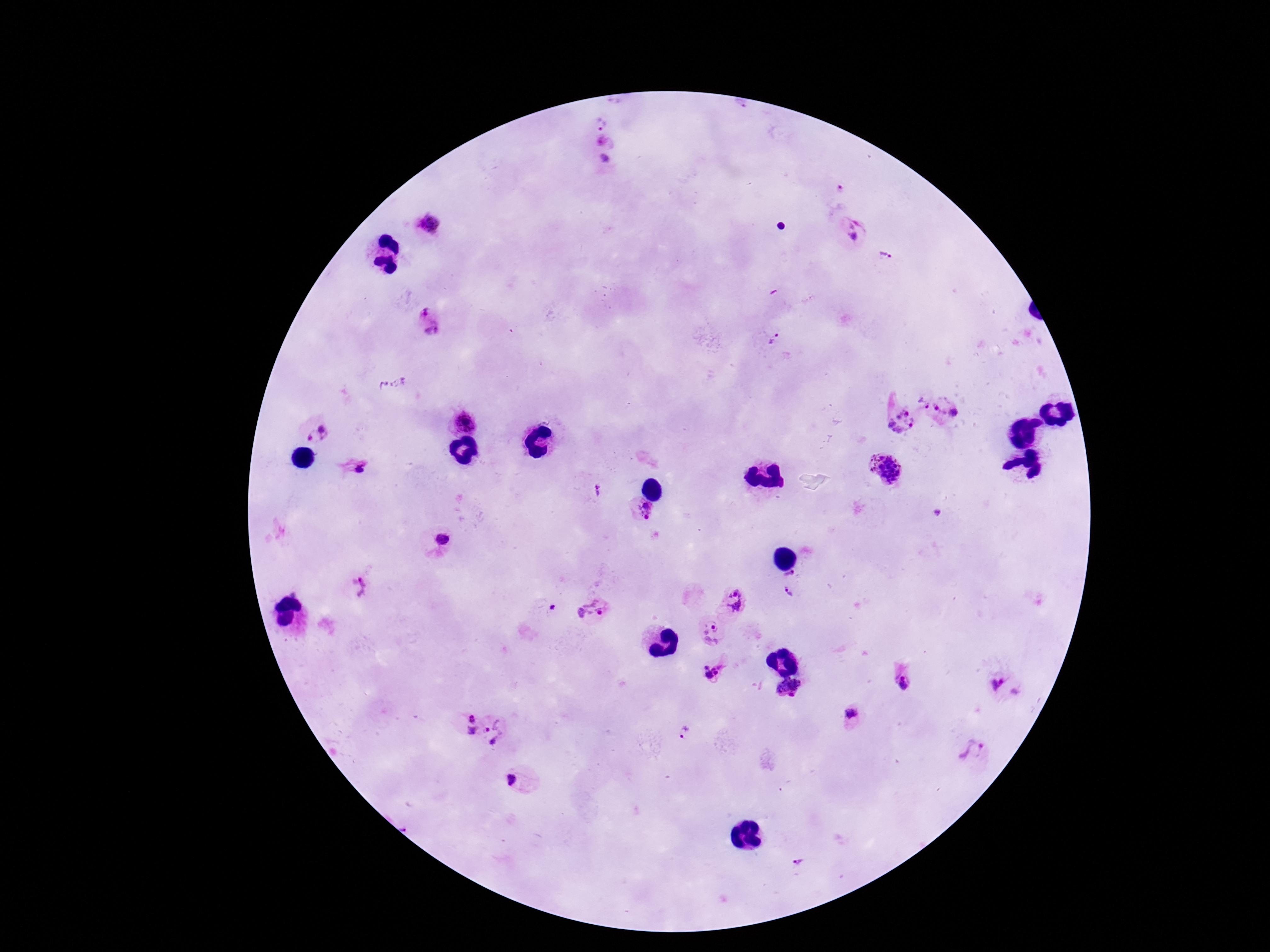

Approximate centers as [x, y] in pixels.
Summary:
  - Plasmodium parasite locations: [601, 124], [605, 160], [428, 224], [852, 229], [885, 256], [423, 312], [432, 329], [774, 337], [923, 402], [937, 407], [954, 413], [463, 421], [900, 421], [322, 428], [315, 439], [356, 467], [884, 469], [598, 491], [638, 512], [937, 514], [441, 541], [790, 575], [361, 588], [788, 595], [735, 601], [554, 608], [592, 610], [710, 634], [713, 672], [902, 682], [1000, 685], [789, 689], [852, 713], [471, 717], [494, 722], [471, 730], [684, 732], [494, 743], [973, 753], [514, 779], [798, 863]
  - Patient malaria status: infected
  - Preparation: thick blood film
  - Image size: 1270×952 pixels
  - Field of view: one from this slide
  - Magnification: 100x
  - Stain: Giemsa
  - Capture: smartphone camera through the microscope eyepiece